Outline each Plasmodium falciparum-infected red blood cell.
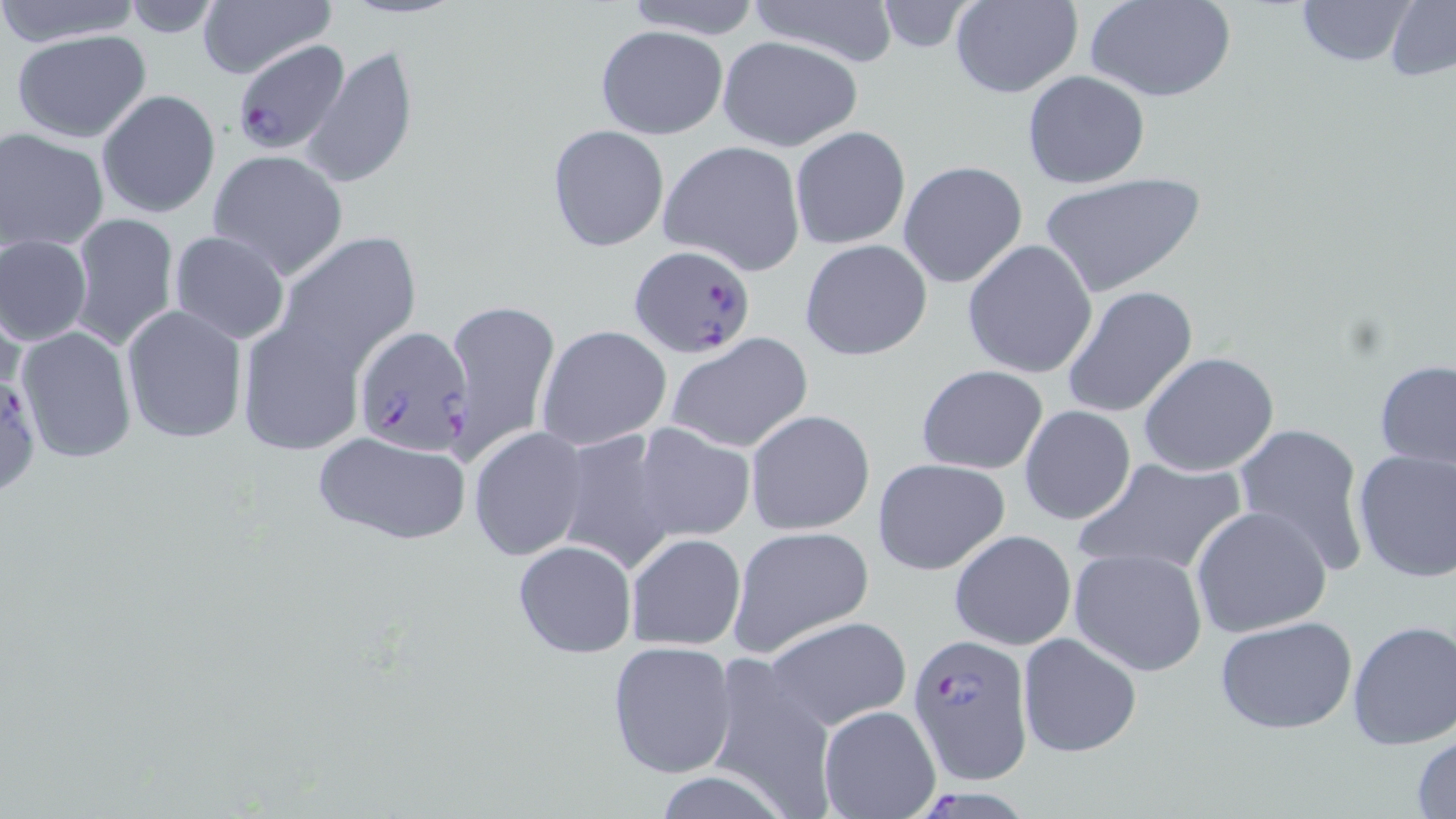
Approximate bounding boxes as (x1, y1, x2, y2) in pixels.
Plasmodium falciparum-infected red blood cells: (233, 40, 346, 154), (626, 244, 757, 359), (353, 324, 475, 455), (0, 364, 41, 498), (905, 636, 1031, 783), (925, 784, 1039, 819).

Summary:
  - Uninfected red blood cell locations: (0, 0, 145, 50), (193, 0, 335, 79), (615, 0, 769, 39), (751, 0, 896, 69), (949, 0, 1082, 99), (1085, 0, 1236, 103), (1292, 0, 1420, 68), (1384, 1, 1456, 82), (870, 2, 981, 53), (595, 24, 727, 139), (9, 29, 152, 143), (717, 35, 864, 153), (302, 44, 417, 191), (1021, 71, 1152, 190), (96, 89, 220, 218), (547, 124, 669, 251), (789, 126, 911, 249), (1, 127, 108, 251), (659, 140, 808, 275), (208, 150, 348, 280), (898, 162, 1028, 288), (1038, 171, 1207, 298), (69, 213, 179, 351), (168, 230, 291, 345), (270, 232, 423, 377), (2, 233, 92, 347), (799, 238, 931, 359), (961, 239, 1097, 379), (1060, 285, 1199, 420), (440, 298, 559, 463), (119, 305, 247, 443), (235, 320, 368, 456), (536, 325, 672, 451), (16, 326, 138, 463), (665, 333, 812, 453), (1138, 352, 1281, 478), (1373, 358, 1456, 479), (917, 364, 1050, 475), (1018, 405, 1136, 526), (744, 409, 875, 536), (1233, 421, 1370, 577), (630, 422, 755, 542), (468, 426, 590, 561), (313, 429, 470, 547), (553, 430, 680, 575), (1352, 449, 1456, 583), (1073, 454, 1248, 577), (872, 456, 1011, 576), (1191, 506, 1333, 639), (728, 527, 875, 656), (947, 530, 1075, 649), (624, 532, 747, 650), (512, 538, 638, 659), (1067, 548, 1209, 677), (760, 616, 913, 733), (1214, 616, 1358, 735), (1346, 619, 1456, 750), (1017, 631, 1142, 758), (607, 640, 737, 778), (700, 655, 840, 817), (818, 703, 942, 818), (1411, 733, 1456, 818), (653, 773, 786, 817)
  - Slide-level diagnosis: Plasmodium falciparum
  - Stain: May-Grünwald-Giemsa
  - Image size: 1456×819 pixels
  - Preparation: thin blood film
  - Magnification: 1000x
  - Field of view: one of a larger specimen
  - Modality: optical microscopy